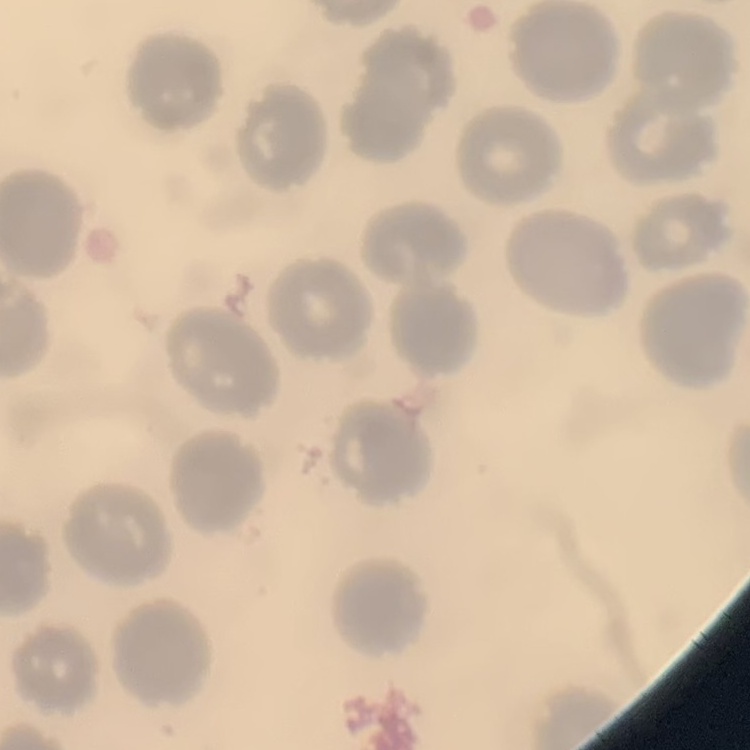
erythrocyte morphology = no rouleaux formation
preparation = thin peripheral smear
image type = square crop of a larger photomicrograph
stain = Field's or Giemsa